Report the malaria status of this cell.
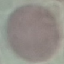
It is uninfected.

image type = cell patch, automatically extracted from a larger field of view and resized to 64 × 64 pixels
capture = smartphone through the microscope eyepiece
preparation = thin blood film
stain = Giemsa